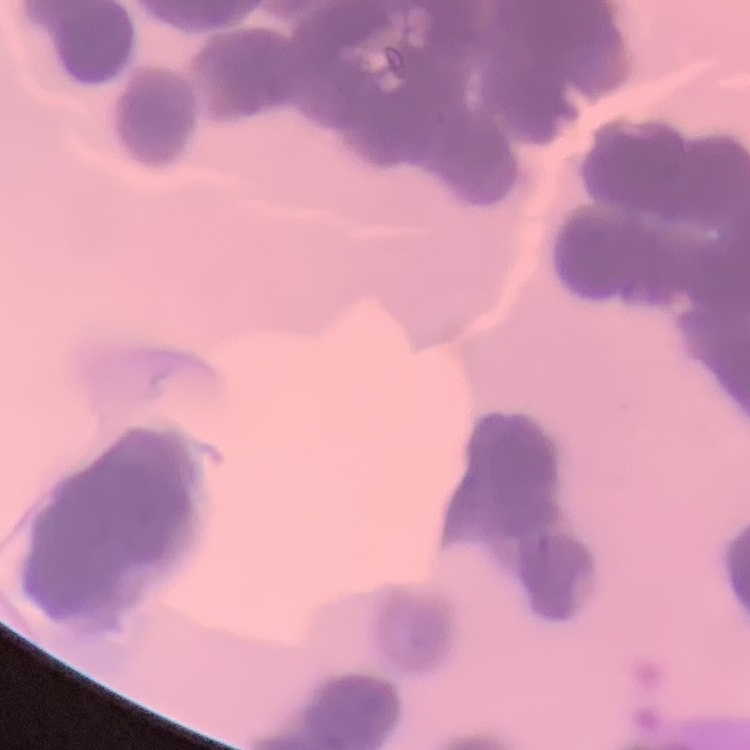

The red blood cells show rouleaux formation. Thin blood smear. One tile cut from a larger photomicrograph. Field's or Giemsa stain.